Locate every blood parasite and identify its species.
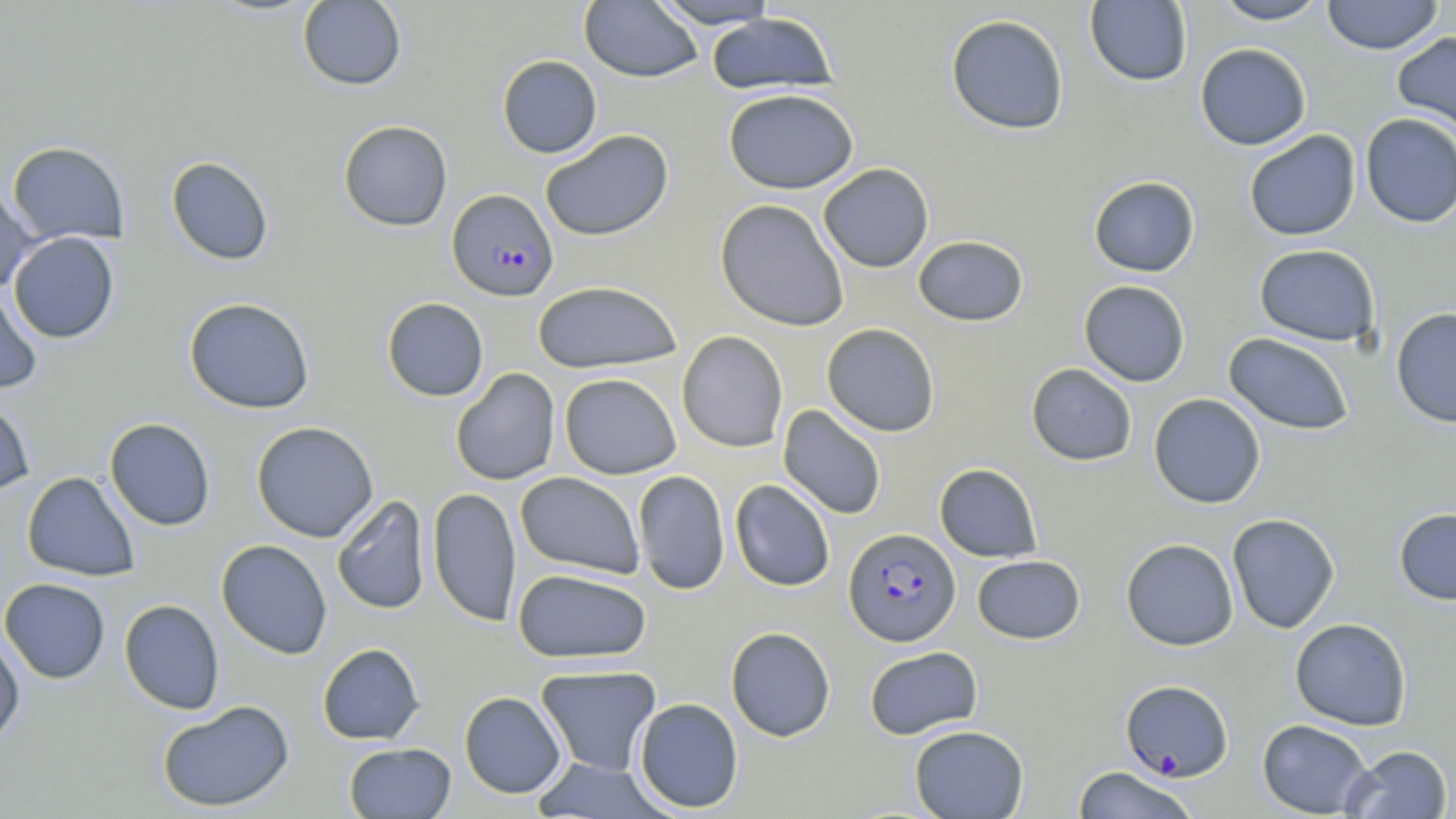
Approximate bounding boxes as named x1/y1/x2/y2 corners in pixels.
Plasmodium falciparum-infected red blood cells: (x1=447, y1=188, x2=558, y2=302), (x1=843, y1=527, x2=960, y2=646), (x1=1120, y1=680, x2=1234, y2=782).
No Plasmodium ovale, Plasmodium malariae, Plasmodium vivax, Babesia divergens, or Trypanosoma brucei observed.

Uninfected red blood cell locations: (x1=296, y1=0, x2=407, y2=90), (x1=580, y1=0, x2=702, y2=82), (x1=648, y1=0, x2=782, y2=29), (x1=1213, y1=0, x2=1331, y2=25), (x1=1321, y1=0, x2=1444, y2=55), (x1=1084, y1=1, x2=1192, y2=87), (x1=706, y1=12, x2=838, y2=94), (x1=945, y1=13, x2=1070, y2=135), (x1=1392, y1=30, x2=1456, y2=140), (x1=1194, y1=43, x2=1311, y2=150), (x1=497, y1=55, x2=602, y2=158), (x1=723, y1=88, x2=859, y2=194), (x1=1360, y1=113, x2=1456, y2=228), (x1=338, y1=120, x2=453, y2=231), (x1=539, y1=129, x2=674, y2=242), (x1=1244, y1=130, x2=1361, y2=241), (x1=6, y1=141, x2=129, y2=246), (x1=166, y1=156, x2=274, y2=265), (x1=818, y1=163, x2=934, y2=272), (x1=1089, y1=176, x2=1200, y2=277), (x1=0, y1=184, x2=37, y2=293), (x1=715, y1=199, x2=849, y2=332), (x1=9, y1=231, x2=119, y2=343), (x1=913, y1=235, x2=1029, y2=327), (x1=1254, y1=244, x2=1381, y2=346), (x1=532, y1=280, x2=682, y2=374), (x1=1078, y1=280, x2=1191, y2=387), (x1=0, y1=287, x2=43, y2=395), (x1=184, y1=297, x2=315, y2=414), (x1=382, y1=297, x2=489, y2=401), (x1=1390, y1=306, x2=1456, y2=427), (x1=822, y1=323, x2=940, y2=437), (x1=676, y1=330, x2=788, y2=453), (x1=1223, y1=332, x2=1355, y2=435), (x1=1026, y1=363, x2=1138, y2=466), (x1=450, y1=368, x2=560, y2=486), (x1=559, y1=373, x2=682, y2=479), (x1=1148, y1=393, x2=1266, y2=508), (x1=0, y1=395, x2=36, y2=499), (x1=778, y1=405, x2=887, y2=520), (x1=104, y1=418, x2=216, y2=531), (x1=251, y1=421, x2=379, y2=542), (x1=934, y1=463, x2=1043, y2=562), (x1=632, y1=470, x2=730, y2=595), (x1=21, y1=471, x2=140, y2=582), (x1=515, y1=472, x2=645, y2=579), (x1=730, y1=480, x2=835, y2=592), (x1=427, y1=486, x2=522, y2=627), (x1=331, y1=495, x2=431, y2=615), (x1=1393, y1=507, x2=1456, y2=605), (x1=1226, y1=513, x2=1341, y2=634), (x1=1120, y1=538, x2=1239, y2=651), (x1=216, y1=539, x2=333, y2=659), (x1=972, y1=554, x2=1085, y2=644), (x1=512, y1=568, x2=652, y2=664), (x1=0, y1=578, x2=111, y2=684), (x1=119, y1=599, x2=225, y2=715), (x1=1289, y1=617, x2=1413, y2=731), (x1=726, y1=626, x2=836, y2=742), (x1=0, y1=632, x2=25, y2=749), (x1=317, y1=643, x2=425, y2=745), (x1=863, y1=646, x2=983, y2=740), (x1=536, y1=665, x2=662, y2=777), (x1=459, y1=691, x2=566, y2=798), (x1=634, y1=697, x2=744, y2=814), (x1=156, y1=699, x2=295, y2=813), (x1=1257, y1=719, x2=1373, y2=818), (x1=909, y1=724, x2=1029, y2=818), (x1=343, y1=742, x2=456, y2=818), (x1=1341, y1=744, x2=1453, y2=818), (x1=530, y1=758, x2=674, y2=818), (x1=1071, y1=766, x2=1201, y2=819). Slide-level diagnosis: Plasmodium falciparum. May-Grünwald-Giemsa-stained preparation. Single field of view. Optical microscopy. Image is 1456×819 pixels. Thin blood smear. Captured at 1000x magnification.